Classify this cell by malaria status.
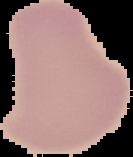

Uninfected.

The area outside the segmented cell region is set to black. From a thin blood smear. Image is 133×157 pixels.